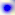
Summary:
  - Magnification: 400x
  - Identification: Toxoplasma gondii
  - Modality: photomicrograph